Mark where platelets are.
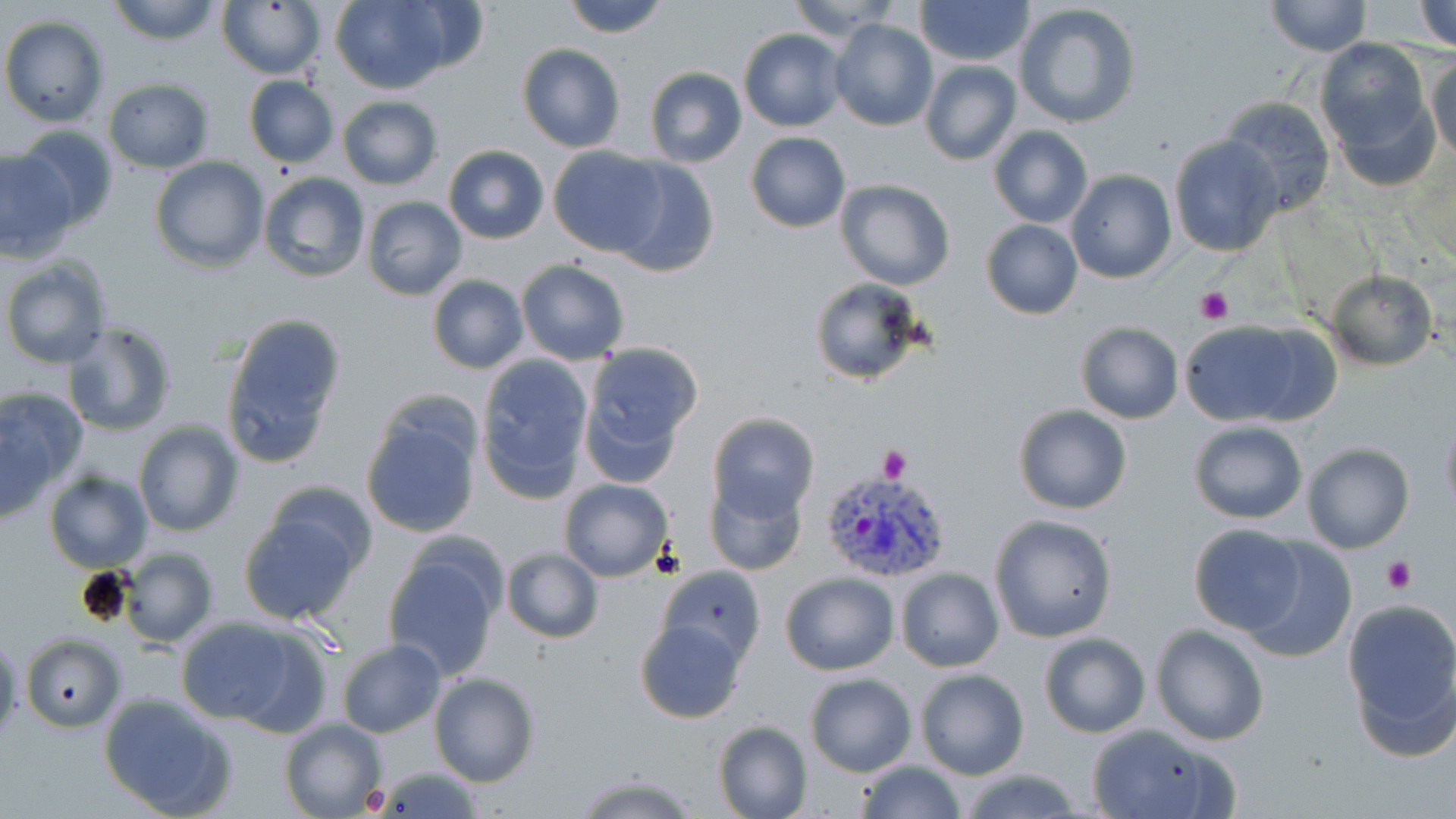

Approximate bounding boxes as (x1,y1)-(x2,y2) corner pairs in pixels.
Platelets: (1194,284)-(1235,325), (876,444)-(911,484), (1381,555)-(1417,594), (357,779)-(392,815).

{
  "plasmodium_vivax_infected_red_blood_cell_locations": "approximate bounding boxes as (x1,y1)-(x2,y2) corner pairs in pixels: (822,469)-(951,585)",
  "slide_level_diagnosis": "Plasmodium vivax",
  "preparation": "thin blood smear",
  "uninfected_red_blood_cell_locations": "approximate bounding boxes as (x1,y1)-(x2,y2) corner pairs in pixels: (106,0)-(225,46), (561,0)-(672,38), (783,0)-(904,42), (917,0)-(1032,66), (1264,0)-(1369,57), (1412,0)-(1456,50), (329,1)-(458,94), (216,2)-(326,78), (1014,2)-(1141,129), (1,16)-(109,126), (828,18)-(937,131), (737,28)-(847,132), (1315,38)-(1437,170), (516,43)-(625,152), (1426,53)-(1456,163), (919,61)-(1021,167), (644,66)-(748,168), (243,75)-(339,169), (102,79)-(215,173), (336,94)-(442,190), (1219,95)-(1337,215), (10,125)-(121,228), (988,126)-(1094,228), (745,131)-(850,233), (1168,134)-(1283,258), (442,144)-(550,244), (548,147)-(667,258), (0,149)-(77,260), (150,157)-(270,272), (609,158)-(719,278), (1065,170)-(1177,285), (257,171)-(371,283), (836,180)-(956,290), (361,196)-(467,300), (981,219)-(1082,320), (2,256)-(115,369), (516,259)-(629,364), (1323,271)-(1438,370), (427,275)-(529,375), (808,276)-(929,387), (219,313)-(345,466), (1175,319)-(1327,426), (1073,320)-(1184,423), (62,321)-(178,436), (581,342)-(703,473), (473,353)-(594,502), (0,387)-(89,514), (361,402)-(482,540), (1012,404)-(1133,514), (1439,404)-(1456,522), (707,413)-(820,520), (133,420)-(244,537), (1187,420)-(1309,524), (1302,442)-(1414,553), (44,470)-(153,573), (706,474)-(808,576), (253,478)-(378,586), (557,478)-(674,582), (237,507)-(365,626), (989,513)-(1117,644), (1187,523)-(1308,634), (1240,541)-(1358,664), (117,547)-(220,646), (500,548)-(603,644), (381,549)-(502,680), (656,564)-(765,666), (895,568)-(1003,674), (780,572)-(899,676), (1341,601)-(1456,750), (173,615)-(327,731), (635,619)-(747,724), (1151,625)-(1269,746), (0,631)-(24,743), (1039,633)-(1151,738), (20,634)-(124,732), (337,638)-(446,739), (916,669)-(1029,780), (429,671)-(540,787), (803,674)-(918,778), (99,693)-(237,819), (279,716)-(386,819), (712,720)-(811,819), (1085,723)-(1237,819), (856,760)-(966,819), (368,766)-(485,816), (958,767)-(1087,819), (571,773)-(701,818)",
  "modality": "optical microscopy",
  "image_size": "1456×819 pixels",
  "magnification": "1000x",
  "stain": "May-Grünwald-Giemsa",
  "field_of_view": "single"
}